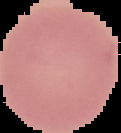 From a thin blood smear. Result: no malaria parasites detected. Cell region segmented out of the field of view; the surrounding area is masked to black. Image is 121×133 pixels.